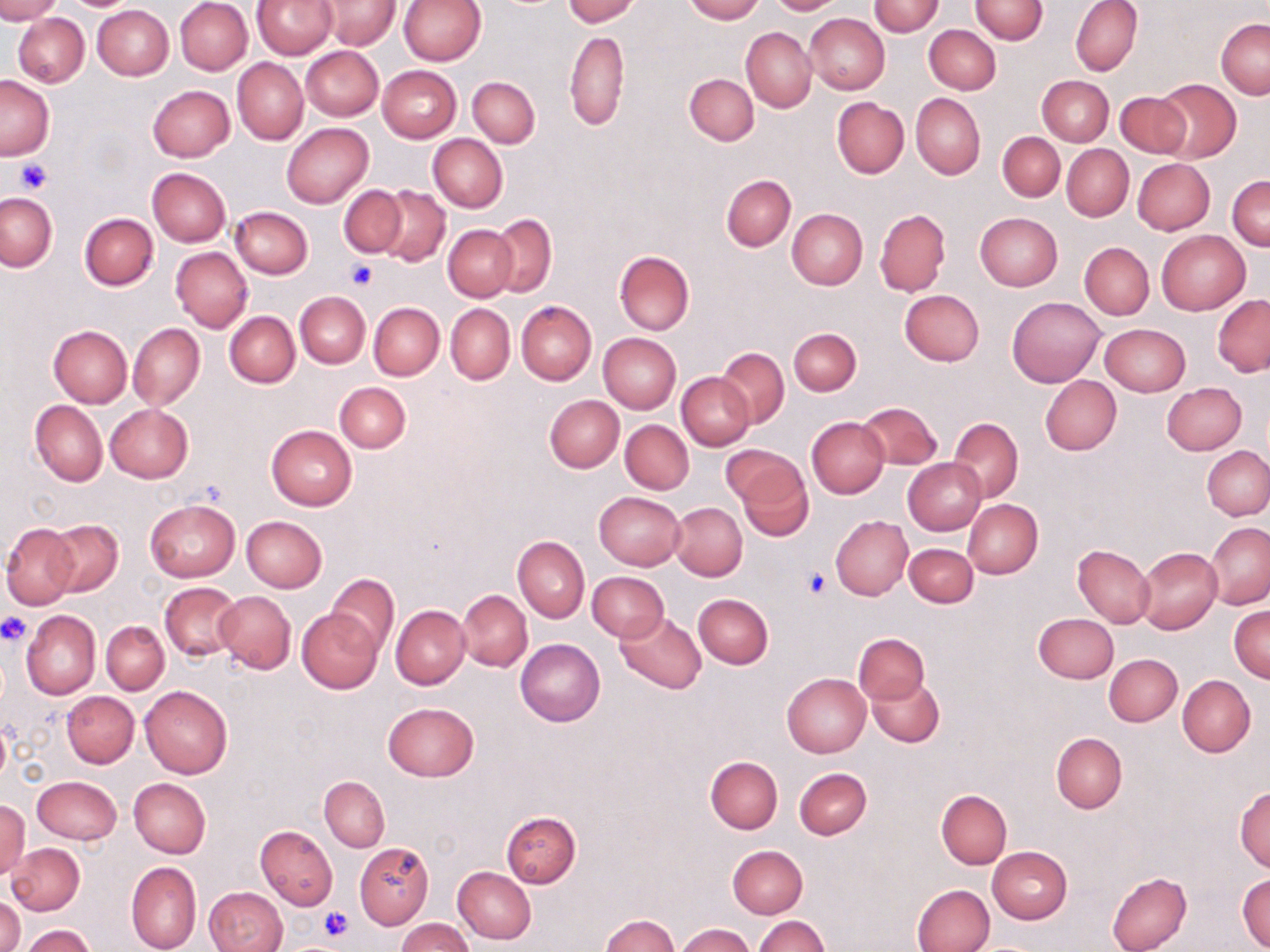

Summary:
  - Coordinate format: approximate bounding boxes as (x1,y1)-(x2,y2) corner pairs in pixels
  - Uninfected red blood cell locations: (0,0)-(61,22), (64,0)-(132,10), (175,0)-(252,75), (253,0)-(335,58), (399,0)-(485,64), (563,0)-(640,25), (682,0)-(764,22), (767,0)-(843,14), (969,0)-(1048,43), (1071,0)-(1142,76), (317,1)-(399,49), (869,1)-(944,36), (92,4)-(174,80), (804,13)-(890,95), (14,14)-(89,87), (1217,19)-(1269,99), (925,25)-(1001,93), (742,27)-(816,113), (564,30)-(629,129), (300,46)-(384,120), (233,58)-(308,145), (377,65)-(461,143), (685,73)-(759,145), (0,75)-(53,160), (1038,75)-(1113,145), (468,76)-(539,148), (1153,79)-(1240,162), (148,85)-(235,162), (1116,90)-(1191,157), (911,92)-(985,179), (831,97)-(908,178), (282,122)-(373,208), (998,131)-(1065,202), (427,133)-(508,212), (1062,145)-(1134,221), (1133,158)-(1215,235), (148,168)-(230,246), (721,174)-(796,251), (1228,175)-(1269,251), (338,185)-(407,257), (374,185)-(452,267), (1,193)-(57,271), (231,206)-(313,279), (787,209)-(867,289), (875,210)-(950,296), (79,212)-(158,290), (975,212)-(1063,290), (490,214)-(557,296), (443,225)-(517,301), (1156,231)-(1249,314), (1080,242)-(1153,319), (170,246)-(251,333), (615,251)-(694,334), (899,290)-(984,366), (295,291)-(369,368), (1213,295)-(1270,377), (1006,297)-(1104,386), (516,301)-(596,385), (369,302)-(444,380), (445,304)-(515,384), (225,311)-(299,387), (1100,323)-(1189,396), (128,324)-(204,411), (49,326)-(132,408), (789,327)-(861,394), (597,332)-(681,413), (717,347)-(788,426), (678,372)-(756,450), (1040,375)-(1121,455), (334,382)-(411,453), (1162,382)-(1247,455), (544,395)-(624,473), (31,401)-(107,486), (857,401)-(942,471), (104,403)-(193,482), (805,416)-(888,498), (949,417)-(1022,501), (611,419)-(690,571), (621,419)-(694,494), (265,424)-(358,510), (720,444)-(806,506), (1202,446)-(1270,521), (731,455)-(815,539), (902,458)-(985,535), (594,491)-(684,570), (964,499)-(1043,578), (146,500)-(239,581), (669,502)-(747,580), (831,515)-(913,599), (242,516)-(327,592), (46,519)-(122,596), (1205,522)-(1270,609), (2,523)-(79,609), (512,535)-(589,622), (904,543)-(978,607), (1073,544)-(1154,627), (1135,547)-(1222,633), (587,571)-(669,641), (327,574)-(398,654), (159,582)-(243,659), (458,590)-(532,671), (215,591)-(296,674), (693,593)-(773,668), (391,605)-(470,689), (1229,605)-(1269,683), (297,607)-(383,694), (20,610)-(100,699), (614,610)-(708,694), (1034,613)-(1118,683), (101,621)-(169,694), (853,632)-(930,706), (515,638)-(604,726), (1103,654)-(1182,727), (782,673)-(871,757), (867,675)-(943,747), (1177,675)-(1255,757), (139,686)-(233,778), (62,691)-(138,767), (383,702)-(479,781), (1051,732)-(1127,813), (706,756)-(782,833), (794,767)-(872,839), (32,776)-(122,844), (319,776)-(389,851), (129,778)-(210,857), (1234,786)-(1270,872), (936,789)-(1012,868), (1,800)-(30,879), (501,811)-(581,887), (255,825)-(337,910), (6,842)-(84,916), (354,842)-(434,928), (726,844)-(808,919), (987,846)-(1072,924), (125,862)-(201,952), (453,867)-(537,944), (1106,871)-(1191,952), (1236,871)-(1270,951), (912,883)-(994,952), (202,887)-(287,952), (1,894)-(23,952), (601,913)-(679,952), (755,916)-(829,952), (396,918)-(473,952), (22,924)-(95,951), (676,924)-(755,952)
  - Platelet locations: (13,157)-(54,195), (344,258)-(379,289), (801,570)-(829,598), (0,613)-(32,645), (317,904)-(354,942)
  - Slide-level diagnosis: negative for blood parasites
  - Image size: 1270×952 pixels
  - Field of view: single
  - Preparation: thin blood smear
  - Modality: light microscopy
  - Magnification: 1000x
  - Stain: May-Grünwald-Giemsa